State which parasite is depicted.
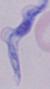

This is a trypanosome.

Micrograph. Captured at 1000x magnification.